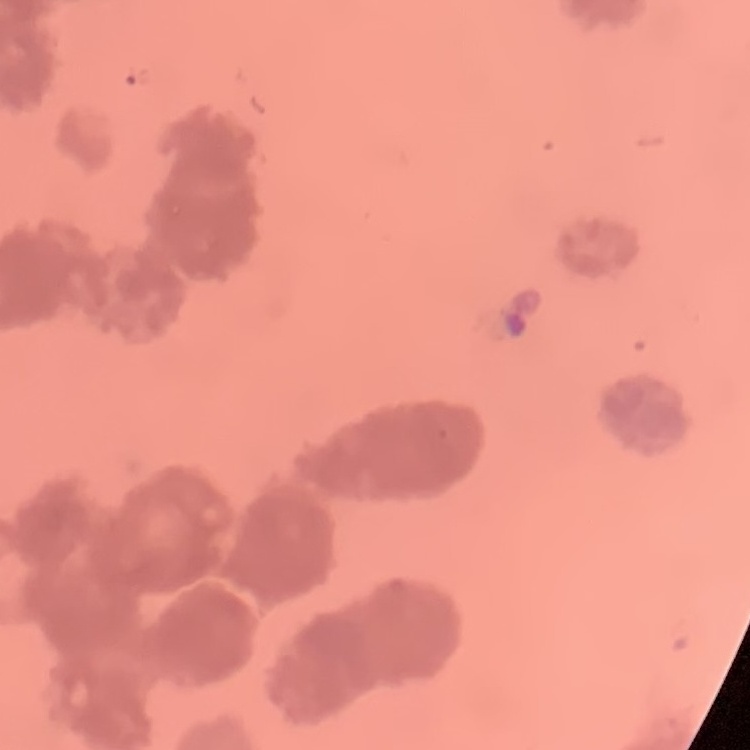

Summary:
  - Red blood cell morphology: rouleaux formation
  - Image type: square crop of a larger photomicrograph
  - Preparation: thin blood smear
  - Stain: Field's or Giemsa